Locate every blood parasite and identify its species.
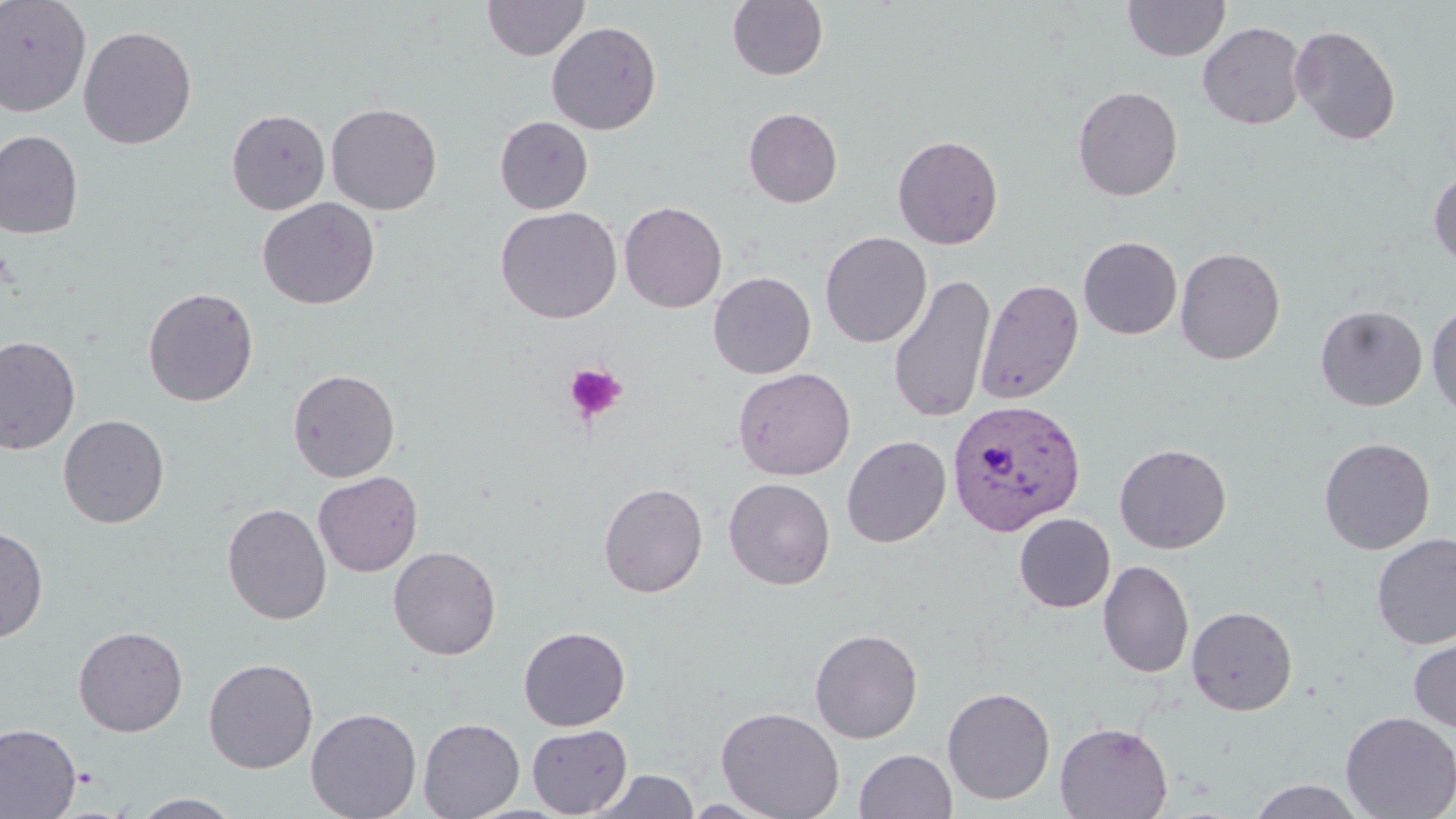
Approximate bounding boxes as named x1/y1/x2/y2 corners in pixels.
Plasmodium vivax-infected red blood cells: (x1=946, y1=398, x2=1086, y2=536).
No Plasmodium falciparum, Plasmodium ovale, Plasmodium malariae, Babesia divergens, or Trypanosoma brucei observed.

Platelet locations: (x1=563, y1=362, x2=627, y2=424). Uninfected red blood cell locations: (x1=0, y1=0, x2=92, y2=117), (x1=483, y1=0, x2=589, y2=61), (x1=727, y1=0, x2=828, y2=81), (x1=1123, y1=0, x2=1230, y2=61), (x1=546, y1=21, x2=662, y2=135), (x1=1197, y1=21, x2=1308, y2=129), (x1=1290, y1=24, x2=1402, y2=145), (x1=79, y1=25, x2=197, y2=149), (x1=1072, y1=86, x2=1183, y2=201), (x1=326, y1=102, x2=443, y2=215), (x1=743, y1=107, x2=843, y2=208), (x1=226, y1=109, x2=331, y2=215), (x1=495, y1=116, x2=593, y2=214), (x1=0, y1=130, x2=84, y2=240), (x1=892, y1=134, x2=1004, y2=250), (x1=1429, y1=169, x2=1456, y2=269), (x1=257, y1=197, x2=380, y2=310), (x1=619, y1=201, x2=727, y2=313), (x1=496, y1=206, x2=623, y2=323), (x1=819, y1=231, x2=932, y2=348), (x1=1078, y1=236, x2=1182, y2=339), (x1=1175, y1=247, x2=1286, y2=365), (x1=708, y1=272, x2=816, y2=378), (x1=887, y1=273, x2=996, y2=424), (x1=976, y1=278, x2=1084, y2=405), (x1=142, y1=286, x2=259, y2=406), (x1=1426, y1=303, x2=1456, y2=419), (x1=1315, y1=304, x2=1428, y2=410), (x1=0, y1=335, x2=81, y2=455), (x1=733, y1=367, x2=856, y2=481), (x1=287, y1=368, x2=401, y2=482), (x1=58, y1=414, x2=169, y2=528), (x1=841, y1=435, x2=951, y2=548), (x1=1318, y1=437, x2=1436, y2=554), (x1=1114, y1=443, x2=1232, y2=554), (x1=313, y1=471, x2=424, y2=576), (x1=723, y1=477, x2=836, y2=590), (x1=598, y1=482, x2=708, y2=597), (x1=222, y1=503, x2=332, y2=625), (x1=1013, y1=513, x2=1116, y2=613), (x1=0, y1=524, x2=49, y2=644), (x1=1371, y1=532, x2=1456, y2=649), (x1=388, y1=546, x2=501, y2=660), (x1=1098, y1=560, x2=1194, y2=679), (x1=1186, y1=605, x2=1298, y2=715), (x1=73, y1=625, x2=188, y2=737), (x1=519, y1=626, x2=631, y2=731), (x1=810, y1=628, x2=924, y2=743), (x1=1408, y1=635, x2=1456, y2=734), (x1=203, y1=658, x2=318, y2=774), (x1=942, y1=686, x2=1055, y2=805), (x1=716, y1=706, x2=845, y2=819), (x1=305, y1=707, x2=422, y2=819), (x1=1340, y1=711, x2=1456, y2=819), (x1=418, y1=717, x2=525, y2=819), (x1=1054, y1=721, x2=1174, y2=818), (x1=0, y1=723, x2=81, y2=819), (x1=527, y1=724, x2=632, y2=817), (x1=854, y1=749, x2=957, y2=819), (x1=588, y1=770, x2=700, y2=818), (x1=1246, y1=779, x2=1367, y2=818), (x1=131, y1=793, x2=243, y2=818), (x1=681, y1=797, x2=787, y2=817). Slide-level diagnosis: Plasmodium vivax. Image is 1456×819 pixels. Thin blood film. Captured at 1000x magnification. May-Grünwald-Giemsa-stained preparation. Light microscopy. One field of a larger specimen.